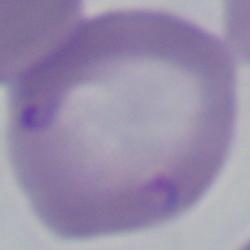 Photomicrograph. A Babesia parasite is shown. 1000x magnification.